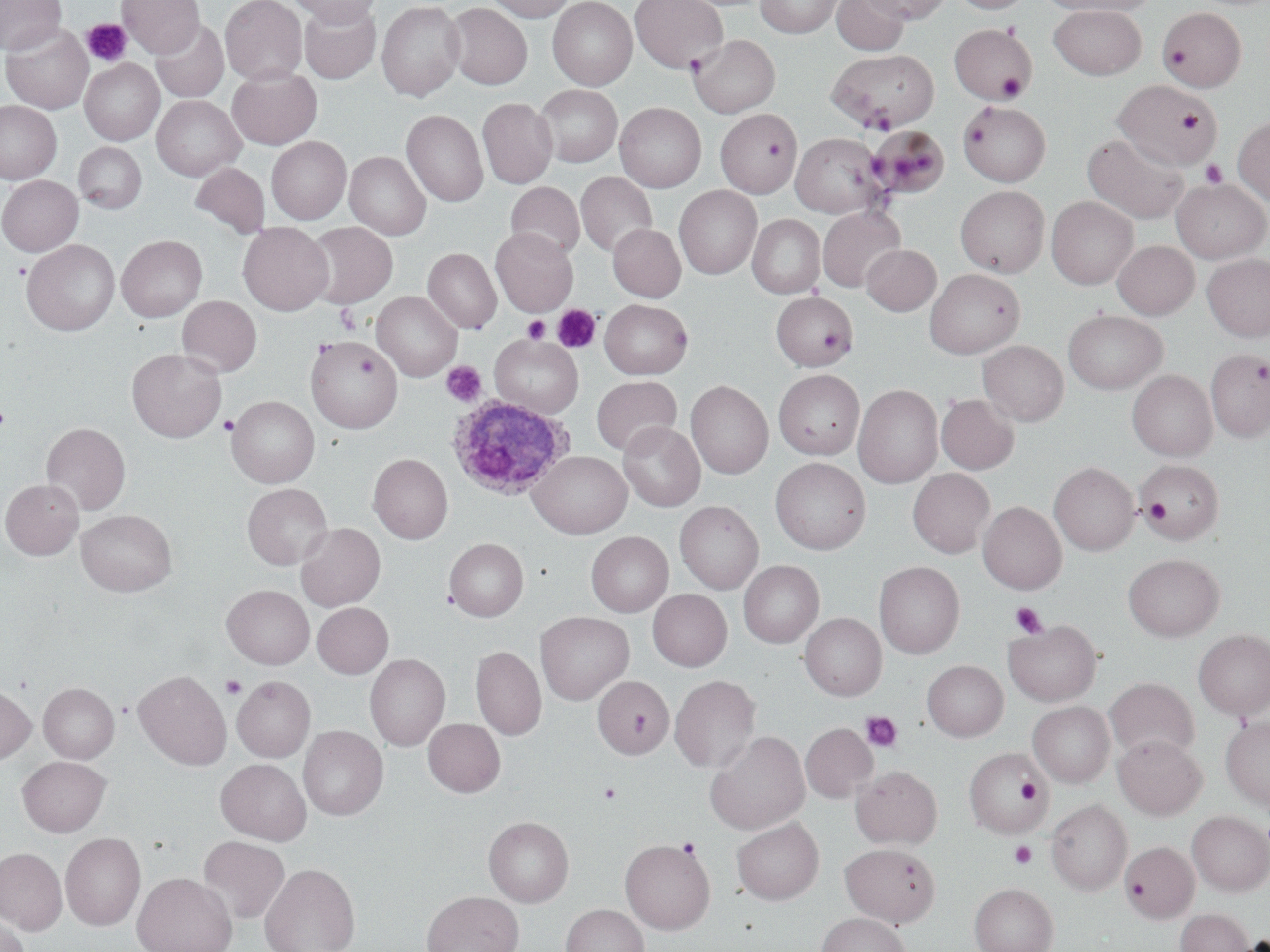

Summary:
  - Coordinate format: approximate bounding boxes as [x1, y1, x2, y2] in pixels
  - Uninfected red blood cell locations: [0, 0, 66, 56], [117, 0, 204, 57], [220, 0, 306, 84], [286, 0, 383, 26], [484, 0, 575, 22], [547, 0, 637, 89], [629, 0, 728, 72], [756, 0, 841, 37], [832, 0, 908, 55], [860, 0, 950, 23], [952, 0, 1032, 14], [1040, 0, 1157, 16], [377, 1, 465, 100], [299, 3, 381, 82], [445, 3, 533, 90], [1049, 6, 1146, 79], [1158, 7, 1246, 91], [150, 19, 228, 102], [1, 22, 93, 114], [949, 24, 1037, 104], [688, 34, 779, 117], [826, 49, 938, 133], [80, 59, 163, 145], [227, 67, 322, 149], [1114, 80, 1221, 169], [535, 85, 622, 167], [152, 95, 245, 180], [477, 97, 557, 188], [959, 100, 1051, 186], [0, 101, 62, 183], [615, 103, 705, 192], [402, 109, 488, 206], [716, 110, 802, 197], [1233, 115, 1270, 205], [867, 126, 949, 199], [1083, 131, 1189, 224], [791, 133, 886, 217], [266, 136, 351, 224], [74, 142, 146, 213], [344, 151, 430, 240], [191, 162, 270, 238], [576, 171, 657, 258], [0, 175, 83, 256], [1172, 178, 1269, 262], [506, 182, 585, 260], [674, 185, 761, 278], [956, 186, 1049, 277], [1046, 196, 1138, 288], [817, 205, 906, 292], [747, 214, 824, 298], [304, 222, 397, 308], [237, 223, 333, 315], [608, 223, 685, 301], [491, 228, 577, 316], [116, 235, 207, 322], [22, 239, 119, 335], [1112, 240, 1199, 320], [861, 245, 940, 316], [423, 248, 501, 333], [1202, 254, 1270, 341], [925, 268, 1025, 359], [372, 292, 462, 381], [772, 292, 857, 371], [177, 295, 262, 378], [600, 299, 693, 379], [1063, 310, 1167, 394], [306, 334, 403, 433], [490, 335, 583, 417], [978, 340, 1068, 426], [127, 348, 227, 443], [1206, 349, 1270, 442], [773, 369, 864, 460], [1128, 370, 1217, 461], [591, 376, 681, 456], [686, 380, 773, 479], [854, 384, 943, 488], [936, 393, 1019, 474], [227, 395, 319, 487], [618, 421, 705, 511], [41, 422, 130, 515], [528, 451, 632, 538], [368, 453, 453, 544], [770, 458, 870, 554], [1137, 460, 1224, 543], [1049, 462, 1139, 555], [908, 468, 995, 558], [0, 479, 83, 559], [242, 483, 333, 570], [674, 501, 763, 594], [978, 501, 1066, 594], [76, 509, 176, 596], [295, 522, 385, 611], [586, 531, 673, 617], [444, 538, 528, 621], [1123, 554, 1224, 641], [738, 560, 824, 648], [874, 561, 964, 658], [222, 585, 314, 668], [648, 589, 732, 671], [312, 602, 393, 678], [535, 611, 634, 704], [800, 612, 886, 700], [1004, 620, 1101, 706], [1194, 629, 1270, 719], [471, 646, 545, 740], [365, 653, 450, 750], [922, 660, 1008, 742], [134, 669, 231, 770], [670, 674, 761, 773], [592, 675, 674, 759], [232, 676, 315, 761], [1105, 677, 1200, 762], [38, 682, 119, 763], [0, 684, 36, 764], [1028, 701, 1114, 787], [682, 703, 785, 815], [1220, 717, 1270, 809], [423, 719, 505, 797], [800, 723, 877, 803], [298, 726, 388, 820], [705, 730, 810, 834], [1113, 735, 1207, 818], [963, 747, 1051, 837], [17, 756, 110, 836], [215, 759, 311, 845], [852, 765, 942, 848], [1046, 799, 1131, 895], [1187, 811, 1270, 895], [483, 816, 574, 906], [731, 816, 823, 904], [61, 832, 145, 930], [198, 836, 290, 924], [619, 837, 716, 934], [1120, 841, 1199, 923], [840, 842, 940, 927], [0, 847, 67, 934], [260, 862, 360, 952], [132, 871, 237, 952], [969, 882, 1058, 952], [422, 890, 523, 952], [560, 904, 649, 952], [1175, 908, 1254, 952], [0, 911, 30, 952], [816, 912, 912, 952]
  - Platelet locations: [81, 18, 132, 67], [996, 72, 1028, 101], [961, 121, 990, 148], [1201, 160, 1228, 188], [12, 261, 30, 279], [335, 303, 361, 333], [552, 304, 602, 352], [522, 315, 549, 343], [441, 361, 486, 406], [0, 405, 11, 430], [219, 416, 238, 436], [1142, 498, 1172, 525], [1011, 602, 1049, 638], [221, 674, 247, 698], [860, 710, 902, 752], [1015, 777, 1044, 804], [598, 782, 621, 803], [677, 838, 700, 859], [1010, 841, 1037, 868]
  - Plasmodium ovale-infected red blood cell locations: [447, 395, 574, 500]
  - Slide-level diagnosis: Plasmodium ovale
  - Stain: May-Grünwald-Giemsa
  - Image size: 1270×952 pixels
  - Magnification: 1000x
  - Preparation: thin blood smear
  - Field of view: single
  - Modality: optical microscopy